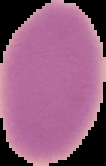

Summary:
  - Image size: 106×166 pixels
  - Malaria status: uninfected
  - Image type: segmented cell region on a black background
  - Preparation: thin blood smear